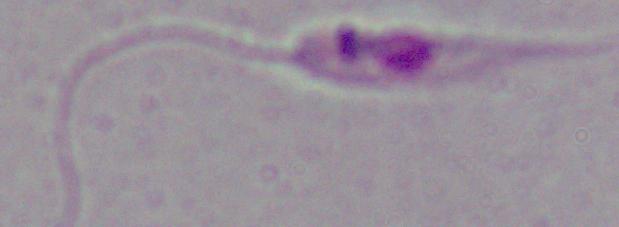
Summary:
  - Magnification: 1000x
  - Identification: Leishmania
  - Modality: photomicrograph